Evaluate for malaria.
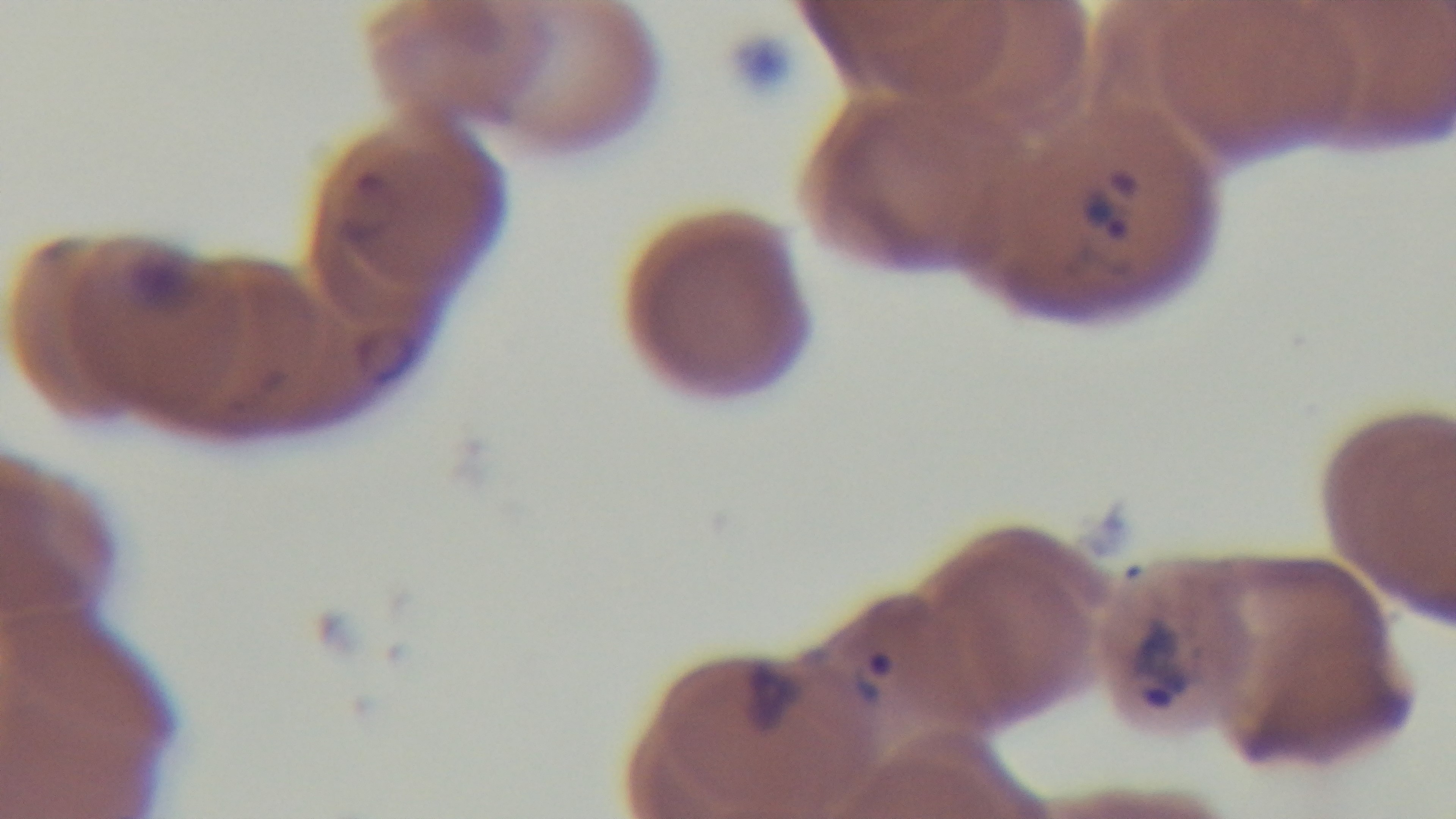
Infected.

objective: 100x oil immersion
modality: light microscopy
field_of_view: single
stain: Giemsa
capture: mounted 4K digital camera
preparation: thin smear